Describe the morphology of the red blood cells.
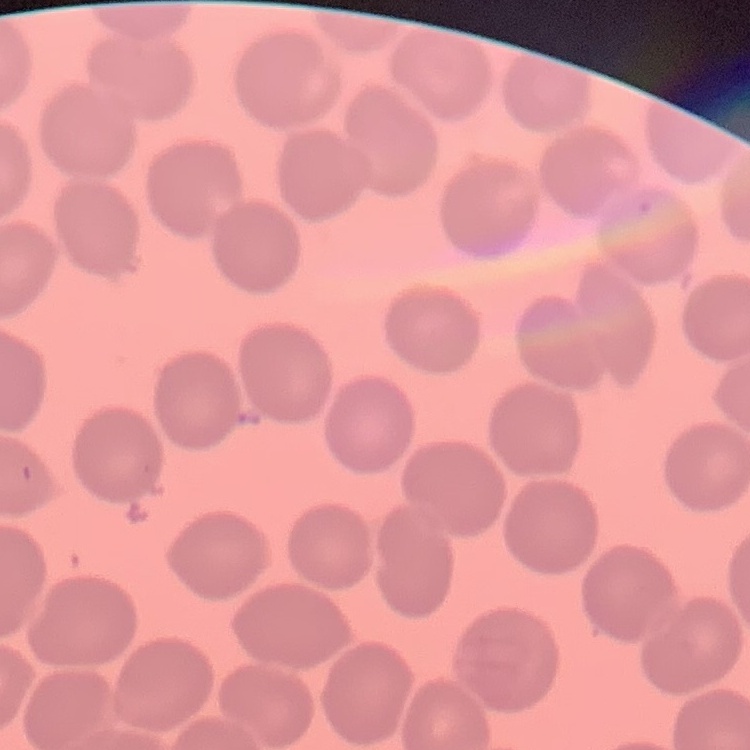

No rouleaux formation.

Stained with either Field's or Giemsa. Thin blood film. One tile cut from a larger photomicrograph.